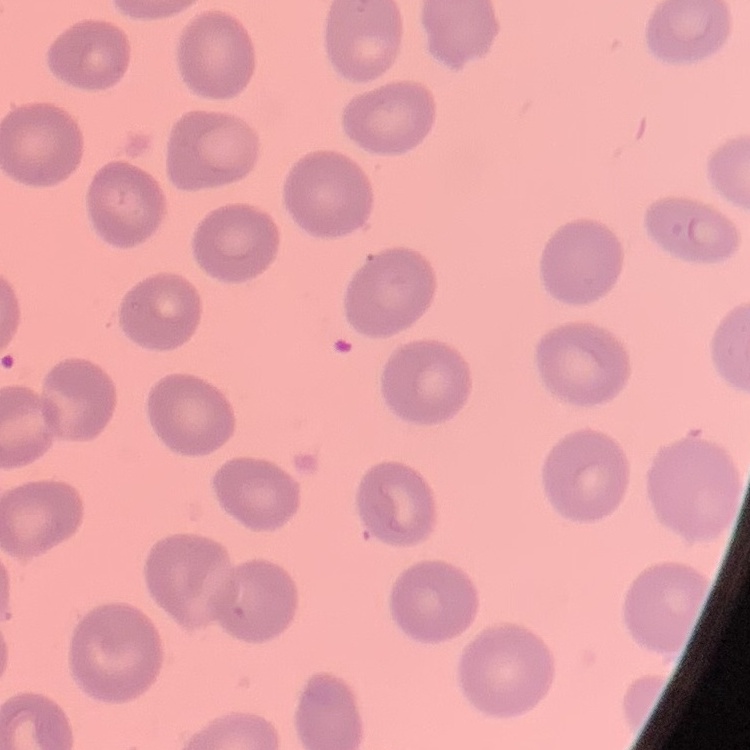

{
  "red_blood_cell_morphology": "no rouleaux formation",
  "image_type": "square crop of a larger photomicrograph",
  "preparation": "thin blood smear",
  "stain": "Field's or Giemsa"
}